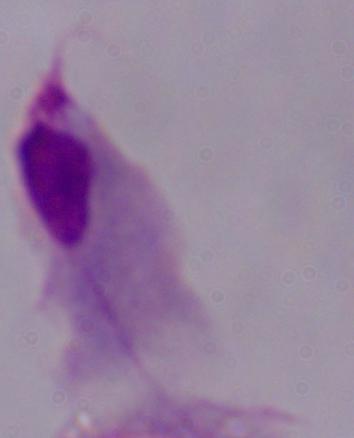

Summary:
  - Modality: micrograph
  - Identification: trichomonad
  - Magnification: 1000x